Comment on the morphology of the erythrocytes.
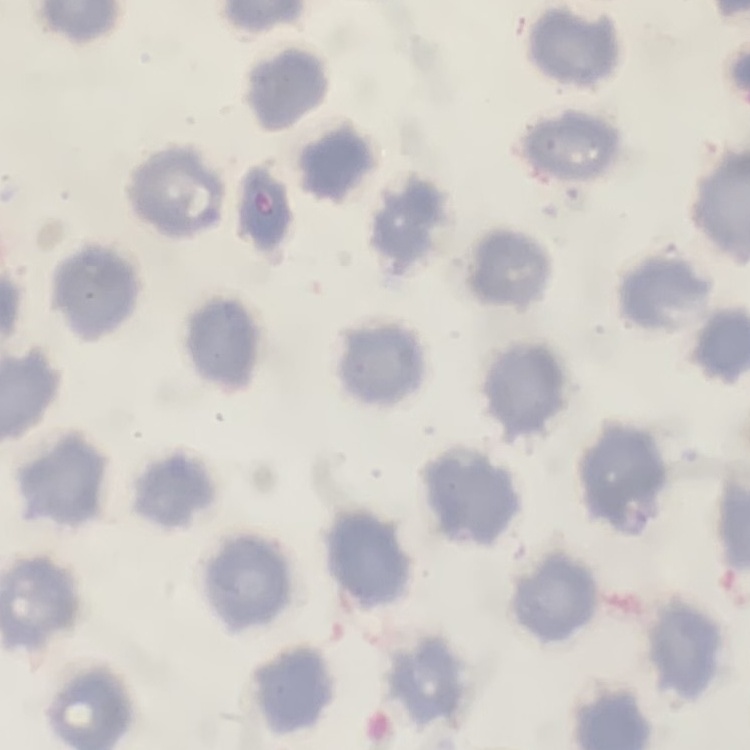
They show no rouleaux formation.

Summary:
  - Image type: square crop of a larger photomicrograph
  - Preparation: thin blood smear
  - Stain: Field's or Giemsa